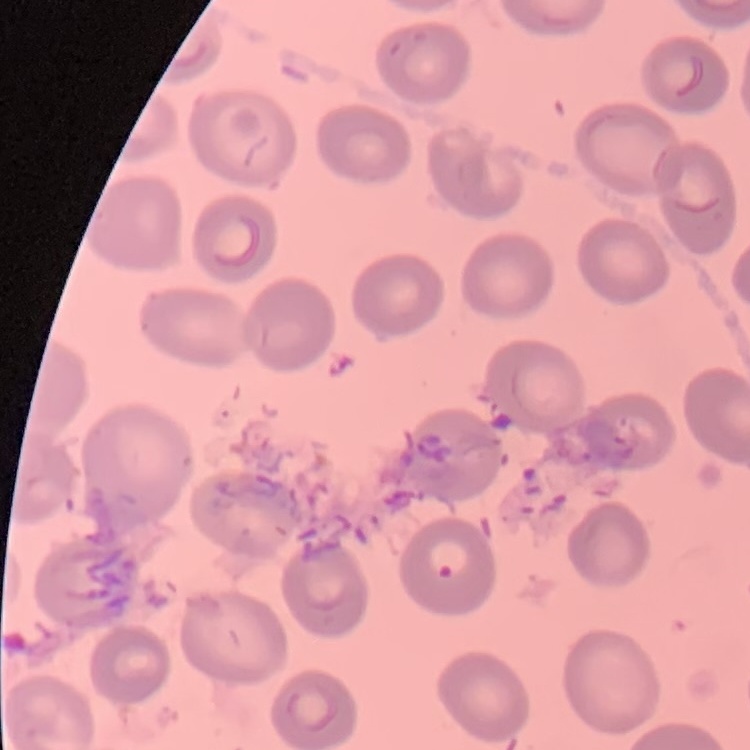

erythrocyte morphology = no rouleaux formation
preparation = thin blood film
image type = square crop of a larger photomicrograph
stain = Field's or Giemsa